Give the extent of all uninfected red blood cells.
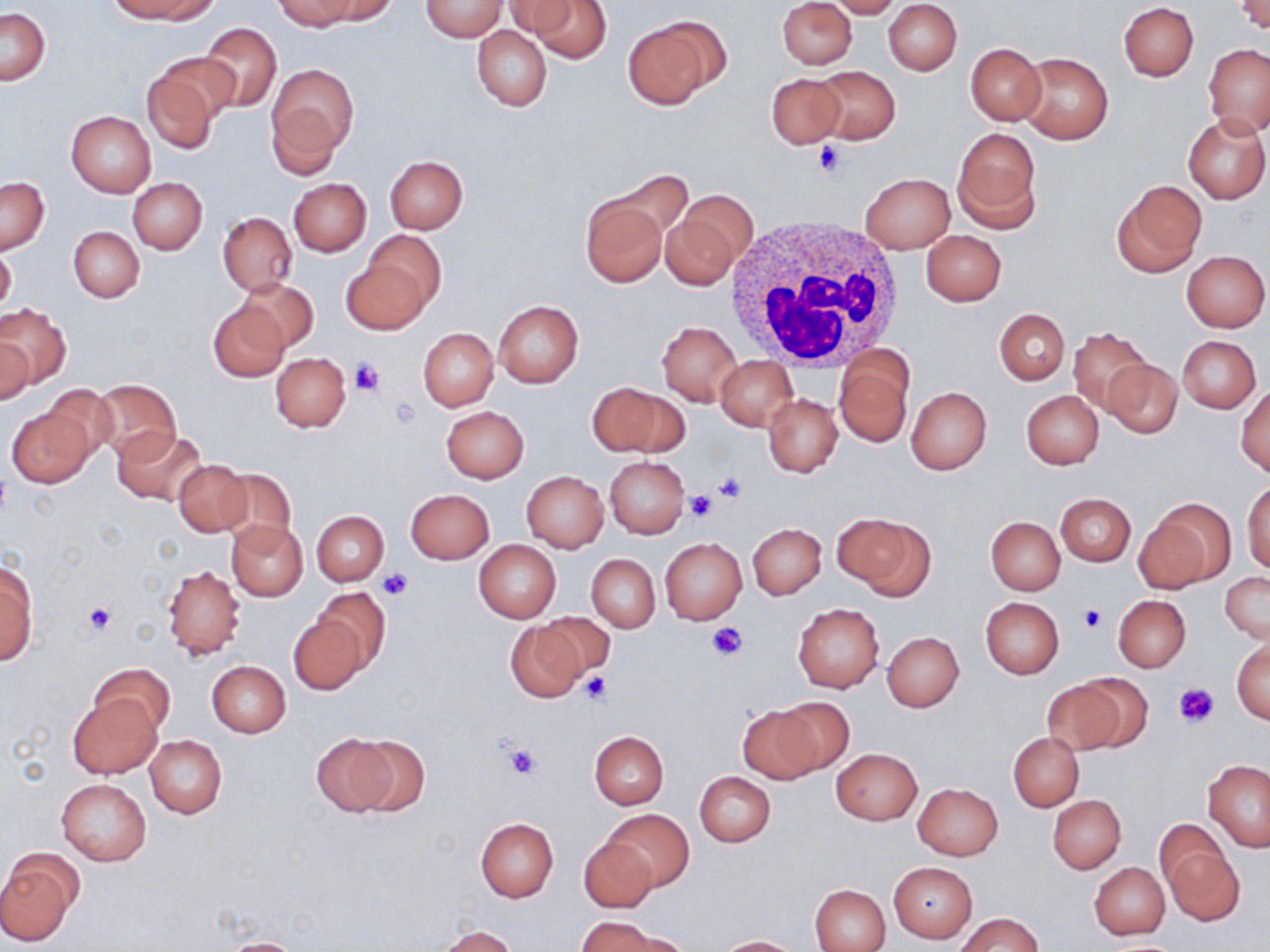

Approximate bounding boxes as (x1, y1, x2, y2) in pixels.
Uninfected red blood cells: (116, 0, 216, 23), (276, 0, 361, 31), (316, 0, 396, 23), (525, 0, 614, 63), (778, 0, 856, 69), (828, 0, 901, 19), (1236, 0, 1269, 32), (421, 1, 507, 40), (503, 1, 579, 39), (884, 1, 962, 75), (1118, 2, 1199, 81), (0, 6, 50, 84), (622, 18, 722, 109), (199, 22, 281, 113), (472, 26, 551, 112), (964, 43, 1046, 126), (1203, 44, 1270, 136), (1017, 50, 1113, 144), (143, 52, 231, 152), (268, 64, 358, 156), (813, 67, 899, 145), (766, 73, 846, 149), (266, 103, 344, 180), (67, 111, 156, 197), (1183, 114, 1269, 204), (954, 128, 1043, 232), (384, 155, 468, 233), (861, 173, 954, 253), (1, 176, 49, 253), (128, 178, 206, 255), (289, 178, 370, 256), (1112, 180, 1206, 276), (579, 194, 667, 287), (663, 195, 750, 281), (218, 213, 296, 295), (68, 226, 144, 302), (362, 229, 445, 315), (920, 230, 1007, 306), (0, 245, 16, 314), (1182, 250, 1269, 331), (341, 255, 431, 335), (237, 277, 320, 353), (493, 301, 584, 388), (208, 302, 288, 381), (0, 305, 71, 389), (995, 308, 1068, 384), (657, 322, 741, 405), (1067, 327, 1154, 417), (418, 328, 497, 411), (0, 333, 35, 407), (1177, 336, 1261, 413), (835, 351, 913, 447), (271, 353, 352, 433), (716, 356, 797, 430), (1102, 360, 1182, 439), (89, 379, 181, 462), (588, 381, 687, 457), (40, 385, 119, 463), (1236, 386, 1270, 477), (907, 387, 991, 474), (1021, 390, 1104, 469), (763, 395, 842, 477), (441, 405, 529, 483), (6, 406, 95, 486), (113, 427, 207, 505), (604, 456, 688, 538), (172, 460, 252, 537), (218, 467, 296, 549), (521, 471, 608, 551), (1243, 483, 1270, 574), (406, 489, 494, 564), (1055, 493, 1136, 566), (1142, 497, 1234, 589), (312, 510, 388, 585), (833, 511, 936, 600), (986, 516, 1065, 596), (226, 520, 308, 601), (748, 523, 825, 599), (660, 538, 747, 624), (473, 540, 561, 622), (586, 554, 660, 632), (1, 562, 37, 665), (162, 564, 244, 660), (1220, 571, 1270, 642), (313, 588, 390, 674), (1113, 595, 1191, 671), (980, 597, 1064, 678), (792, 603, 885, 693), (530, 612, 613, 682), (289, 617, 365, 695), (504, 619, 590, 703), (883, 631, 964, 711), (1231, 638, 1270, 723), (207, 661, 290, 738), (92, 663, 175, 740), (1054, 674, 1148, 756), (67, 693, 162, 779), (772, 695, 854, 775), (736, 703, 827, 785), (590, 731, 669, 809), (1008, 733, 1085, 811), (312, 734, 397, 815), (347, 734, 430, 817), (146, 735, 226, 818), (831, 748, 923, 825), (1203, 759, 1270, 850), (695, 771, 775, 847), (57, 778, 151, 865), (912, 782, 1003, 860), (1047, 794, 1125, 873), (601, 809, 693, 893), (475, 818, 559, 902), (1158, 833, 1243, 924), (578, 836, 658, 913), (1, 852, 78, 943), (1090, 862, 1170, 939), (888, 863, 976, 943), (811, 884, 890, 952), (958, 912, 1043, 952), (576, 917, 668, 951), (430, 926, 520, 951), (714, 935, 800, 951), (216, 937, 310, 951).

Summary:
  - Platelet locations: (813, 139, 844, 179), (350, 357, 383, 397), (389, 397, 421, 431), (712, 473, 746, 503), (684, 490, 716, 521), (376, 567, 413, 601), (82, 601, 116, 636), (1078, 606, 1107, 633), (705, 621, 749, 662), (581, 671, 613, 703), (1174, 682, 1219, 728), (500, 740, 542, 779)
  - White blood cell locations: (724, 216, 906, 374)
  - Slide-level diagnosis: negative for blood parasites
  - Modality: light microscopy
  - Field of view: one of a larger specimen
  - Image size: 1270×952 pixels
  - Stain: May-Grünwald-Giemsa
  - Preparation: thin blood film
  - Magnification: 1000x